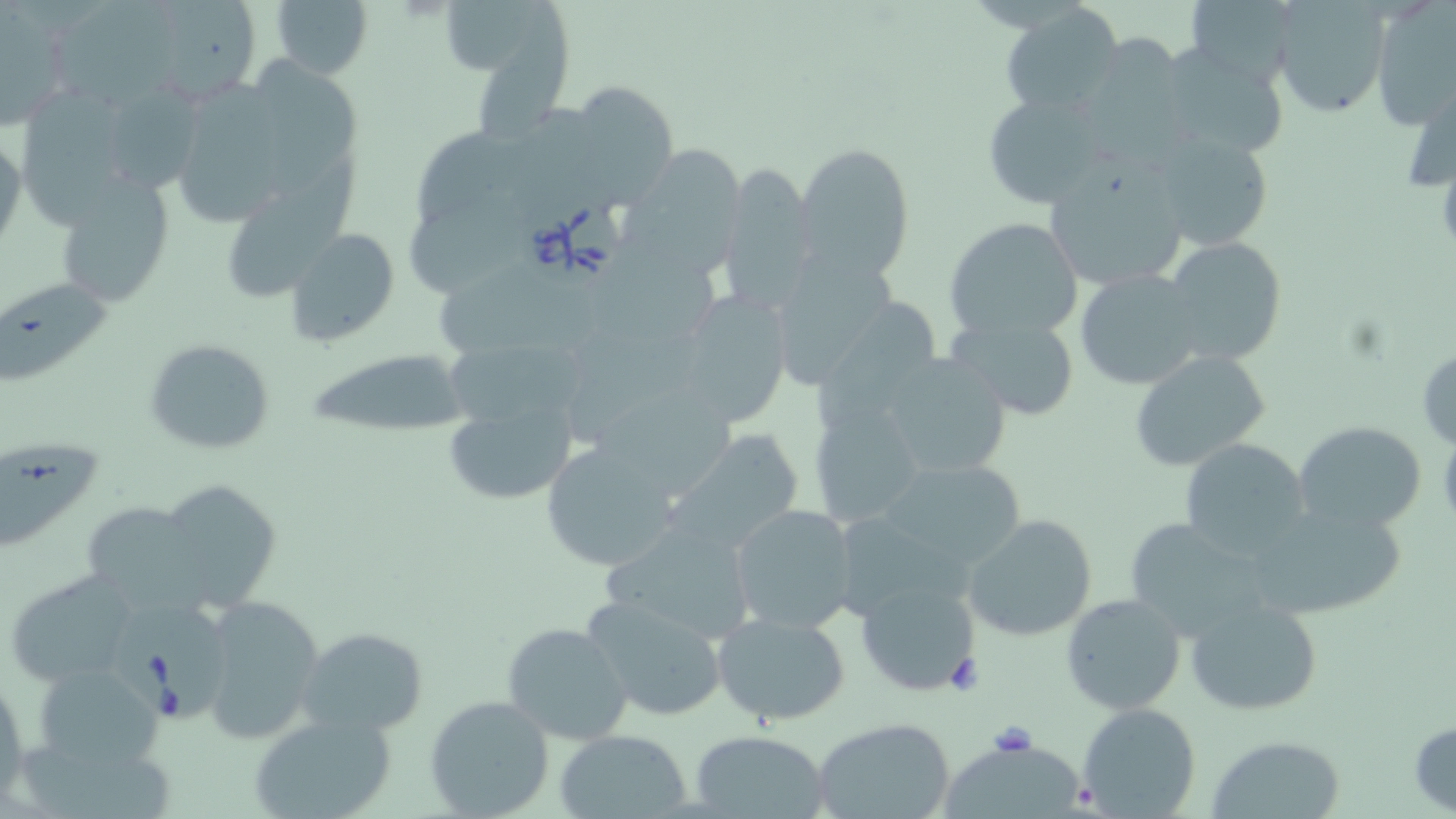

Summary:
  - Coordinate format: approximate bounding boxes as (x1, y1, x2, y2) in pixels
  - Babesia divergens-infected red blood cell locations: (516, 189, 626, 291), (115, 600, 237, 722)
  - Uninfected red blood cell locations: (138, 0, 264, 105), (269, 0, 373, 80), (1185, 0, 1304, 83), (444, 1, 553, 78), (54, 2, 189, 118), (1272, 3, 1389, 119), (1369, 4, 1456, 126), (0, 5, 73, 127), (1001, 5, 1125, 115), (1076, 34, 1189, 157), (1158, 44, 1291, 161), (251, 59, 363, 207), (115, 74, 208, 195), (178, 77, 291, 229), (1406, 78, 1454, 192), (15, 82, 134, 249), (581, 86, 679, 214), (981, 91, 1109, 208), (0, 130, 25, 255), (1149, 130, 1276, 252), (796, 141, 915, 280), (631, 147, 741, 289), (227, 158, 362, 299), (1043, 160, 1192, 294), (717, 162, 821, 313), (56, 174, 176, 306), (406, 187, 533, 304), (942, 217, 1084, 343), (286, 228, 398, 345), (1160, 237, 1287, 365), (779, 242, 915, 393), (1076, 269, 1210, 390), (0, 276, 118, 398), (670, 291, 793, 428), (811, 297, 944, 436), (942, 313, 1082, 420), (445, 329, 590, 440), (143, 338, 275, 455), (1415, 347, 1456, 448), (1127, 348, 1272, 473), (306, 349, 473, 438), (875, 350, 1014, 480), (807, 396, 926, 529), (443, 398, 580, 506), (1293, 420, 1428, 534), (659, 429, 807, 559), (1179, 438, 1311, 560), (539, 441, 680, 571), (0, 445, 106, 556), (877, 455, 1027, 571), (154, 480, 286, 614), (1247, 499, 1409, 624), (88, 500, 209, 626), (728, 503, 858, 635), (962, 514, 1099, 643), (1119, 517, 1278, 639), (599, 519, 760, 645), (5, 570, 144, 687), (854, 574, 984, 697), (579, 592, 731, 723), (1061, 592, 1186, 716), (198, 596, 326, 741), (1185, 598, 1322, 716), (711, 611, 851, 726), (502, 621, 633, 744), (296, 626, 430, 738), (30, 662, 167, 773), (0, 673, 28, 804), (424, 695, 555, 818), (1077, 702, 1201, 818), (247, 712, 396, 819), (812, 717, 959, 819), (1409, 717, 1455, 814), (554, 729, 697, 819), (689, 729, 829, 817), (1211, 735, 1346, 817), (945, 744, 1089, 819)
  - Slide-level diagnosis: Babesia divergens
  - Stain: May-Grünwald-Giemsa
  - Field of view: one of a larger specimen
  - Image size: 1456×819 pixels
  - Magnification: 1000x
  - Preparation: thin blood smear
  - Modality: optical microscopy